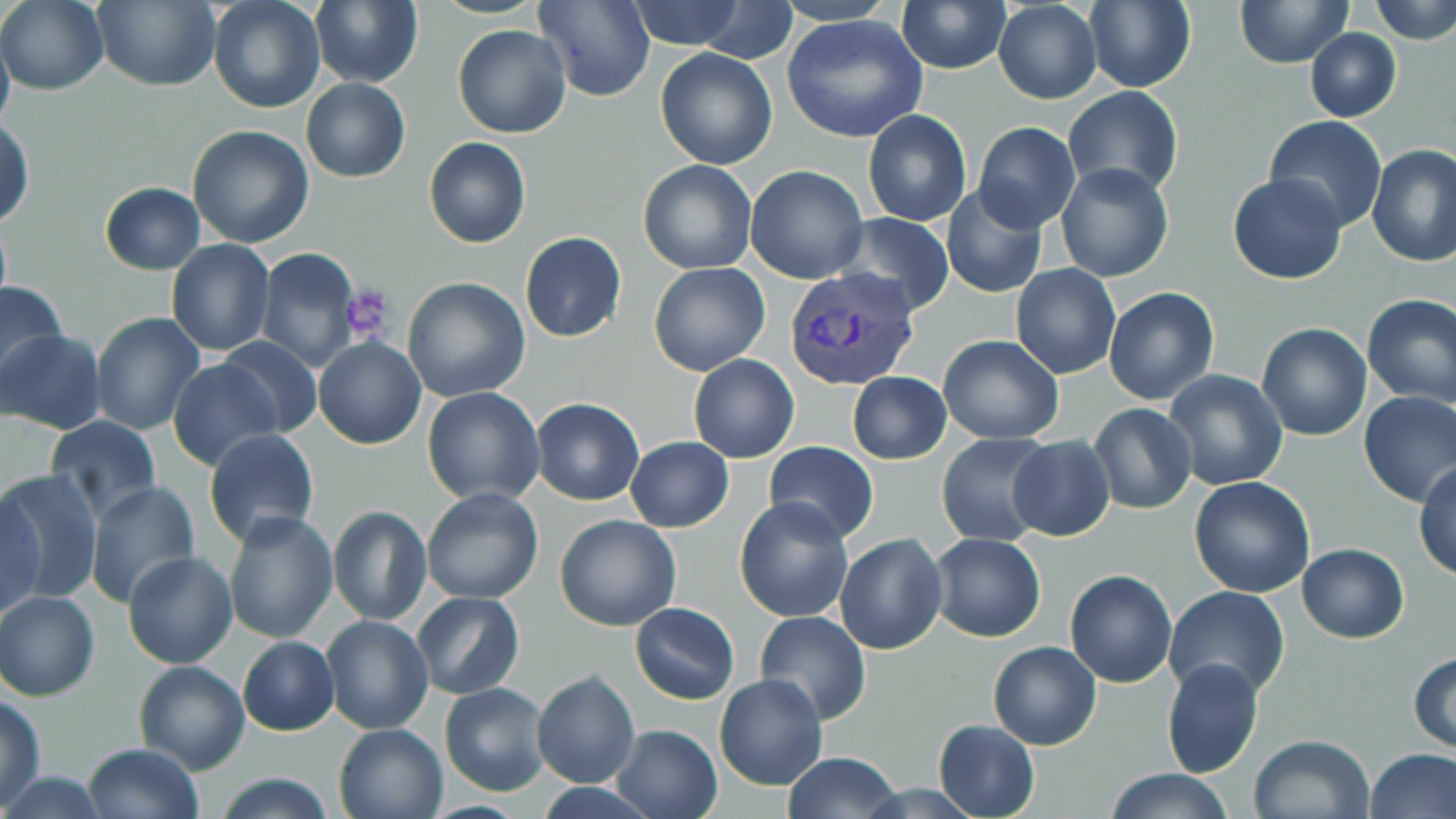
slide-level diagnosis = Plasmodium vivax
preparation = thin blood film
modality = optical microscopy
field of view = one of a larger specimen
platelet locations = approximate bounding boxes as (x1,y1)-(x2,y2) corner pairs in pixels: (340,285)-(397,343)
uninfected red blood cell locations = approximate bounding boxes as (x1,y1)-(x2,y2) corner pairs in pixels: (0,0)-(108,94), (94,0)-(220,92), (208,0)-(324,113), (311,0)-(423,88), (627,0)-(747,50), (686,0)-(801,62), (775,0)-(894,25), (1235,0)-(1352,68), (1369,0)-(1456,45), (534,1)-(657,101), (1083,1)-(1197,93), (897,2)-(1010,74), (993,2)-(1102,104), (781,14)-(929,142), (0,22)-(14,136), (452,24)-(571,139), (1305,27)-(1402,122), (655,48)-(777,170), (300,77)-(411,183), (1064,86)-(1183,199), (863,109)-(971,227), (1264,114)-(1388,232), (0,117)-(34,229), (973,123)-(1080,230), (186,125)-(314,249), (424,137)-(531,249), (1366,142)-(1456,267), (638,160)-(757,274), (1056,162)-(1173,283), (745,165)-(869,283), (1227,173)-(1348,286), (99,182)-(205,275), (939,183)-(1049,299), (834,212)-(956,315), (520,232)-(627,342), (165,238)-(274,356), (256,248)-(361,371), (649,262)-(770,377), (1011,264)-(1121,380), (402,277)-(530,403), (0,278)-(70,389), (1103,286)-(1219,405), (1360,293)-(1455,407), (90,311)-(205,434), (1257,322)-(1372,440), (0,330)-(105,434), (938,334)-(1064,444), (216,337)-(324,437), (314,337)-(425,450), (688,354)-(799,463), (168,359)-(284,471), (1162,369)-(1289,492), (846,371)-(951,464), (422,386)-(545,506), (1358,393)-(1456,508), (531,397)-(644,506), (1088,403)-(1196,515), (45,415)-(161,526), (204,429)-(319,546), (936,432)-(1053,546), (1006,435)-(1116,541), (625,437)-(734,532), (763,440)-(878,543), (1414,461)-(1456,582), (1,467)-(104,601), (1189,476)-(1316,597), (84,482)-(200,609), (422,487)-(543,604), (1,493)-(44,619), (734,496)-(855,623), (327,506)-(434,625), (222,511)-(340,646), (554,513)-(681,632), (929,533)-(1046,642), (836,534)-(947,655), (1298,543)-(1409,643), (123,552)-(238,670), (1065,570)-(1178,688), (1164,585)-(1292,699), (0,590)-(101,702), (411,592)-(525,699), (630,603)-(739,704), (754,611)-(870,723), (320,616)-(432,734), (238,637)-(338,735), (988,641)-(1102,750), (1408,651)-(1456,752), (1162,656)-(1262,777), (134,660)-(249,773), (533,670)-(641,789), (715,673)-(828,791), (440,683)-(550,795), (1,695)-(47,806), (934,720)-(1039,818), (333,721)-(449,819), (611,723)-(724,819), (1248,733)-(1376,819), (80,744)-(203,819), (1367,748)-(1456,819), (783,753)-(904,819), (1104,767)-(1235,819), (1,771)-(111,817), (212,773)-(338,818)
stain = May-Grünwald-Giemsa
Plasmodium vivax-infected red blood cell locations = approximate bounding boxes as (x1,y1)-(x2,y2) corner pairs in pixels: (784,268)-(920,391)
image size = 1456×819 pixels
magnification = 1000x